Point out each Plasmodium parasite.
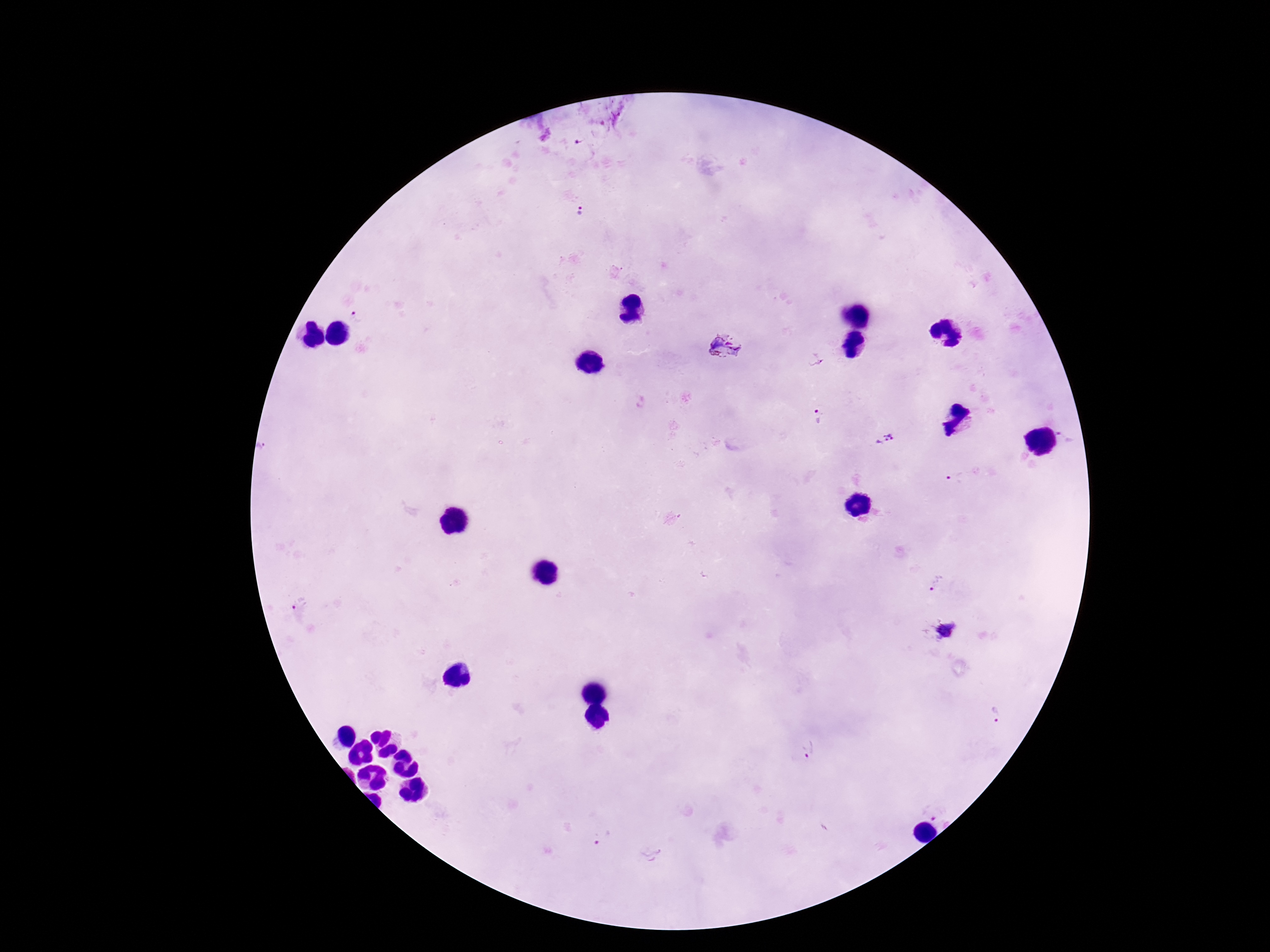

Approximate centers as (x, y) in pixels.
Plasmodium parasites: (581, 142), (582, 215), (357, 315), (727, 349), (816, 361), (817, 416), (1065, 435), (886, 441), (957, 479), (935, 583), (298, 602), (947, 629), (996, 716), (809, 750), (934, 811), (603, 838).

Thick blood smear. Patient malaria status: infected. Image is 1270×952 pixels. Photographed through the microscope eyepiece with a smartphone camera. Giemsa-stained preparation. One field from this slide. 100x magnification.